Identify the parasite.
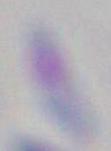
This is Toxoplasma gondii.

{
  "magnification": "1000x",
  "modality": "micrograph"
}